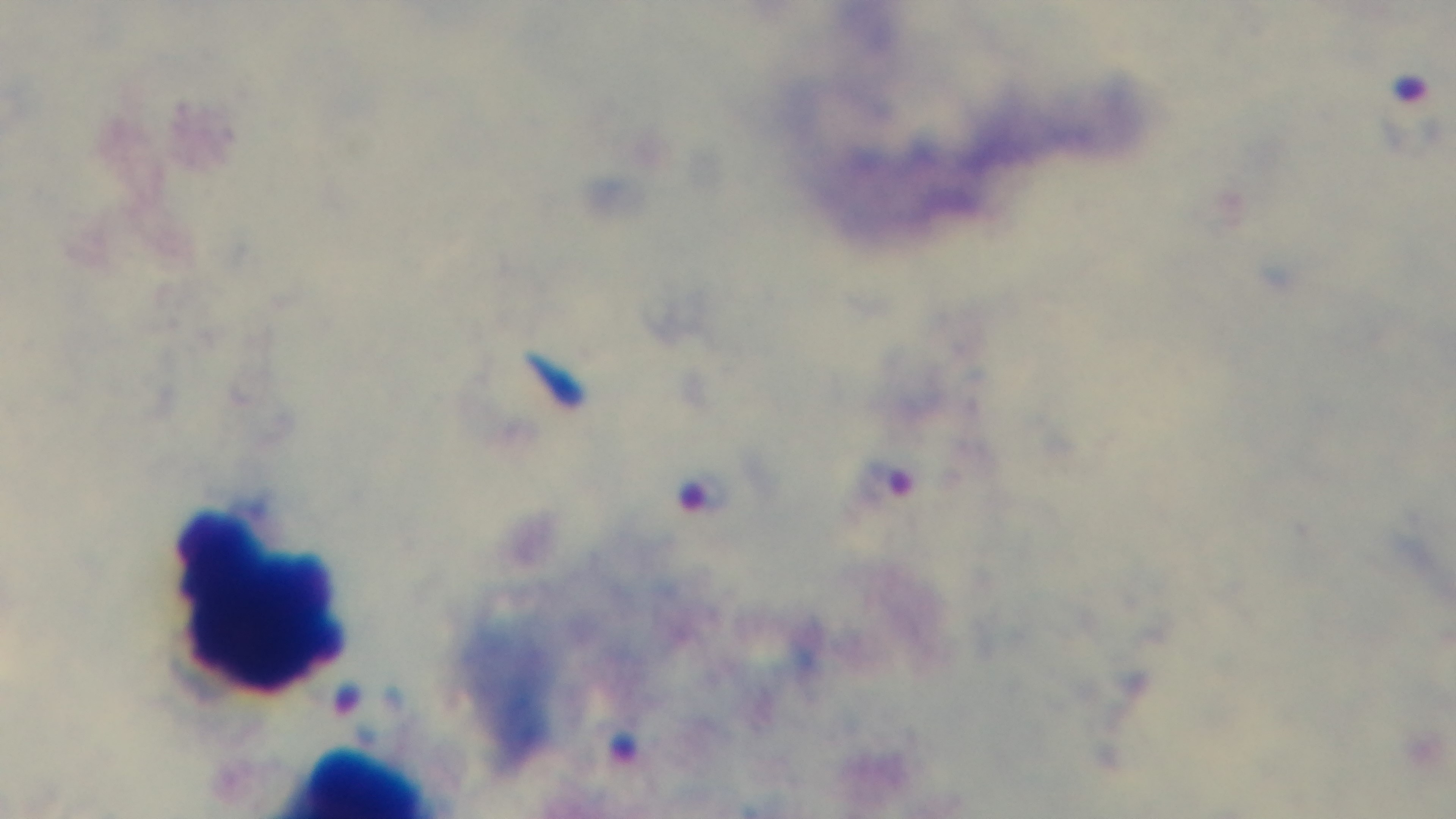

Malaria status: infected. 100x oil-immersion objective. One field from the slide. Captured with a mounted 4K digital camera. Preparation: thick blood film. Light microscopy. Giemsa-stained.